Assess the morphology of the red blood cells.
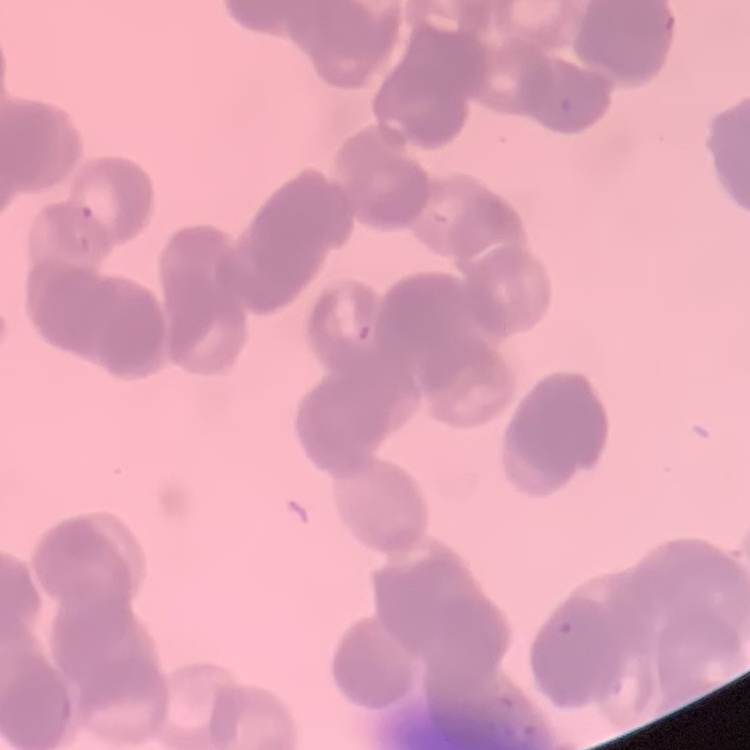

Rouleaux formation.

Square crop of a larger photomicrograph. Thin peripheral smear. Field's or Giemsa stain.